Locate every uninfected red blood cell.
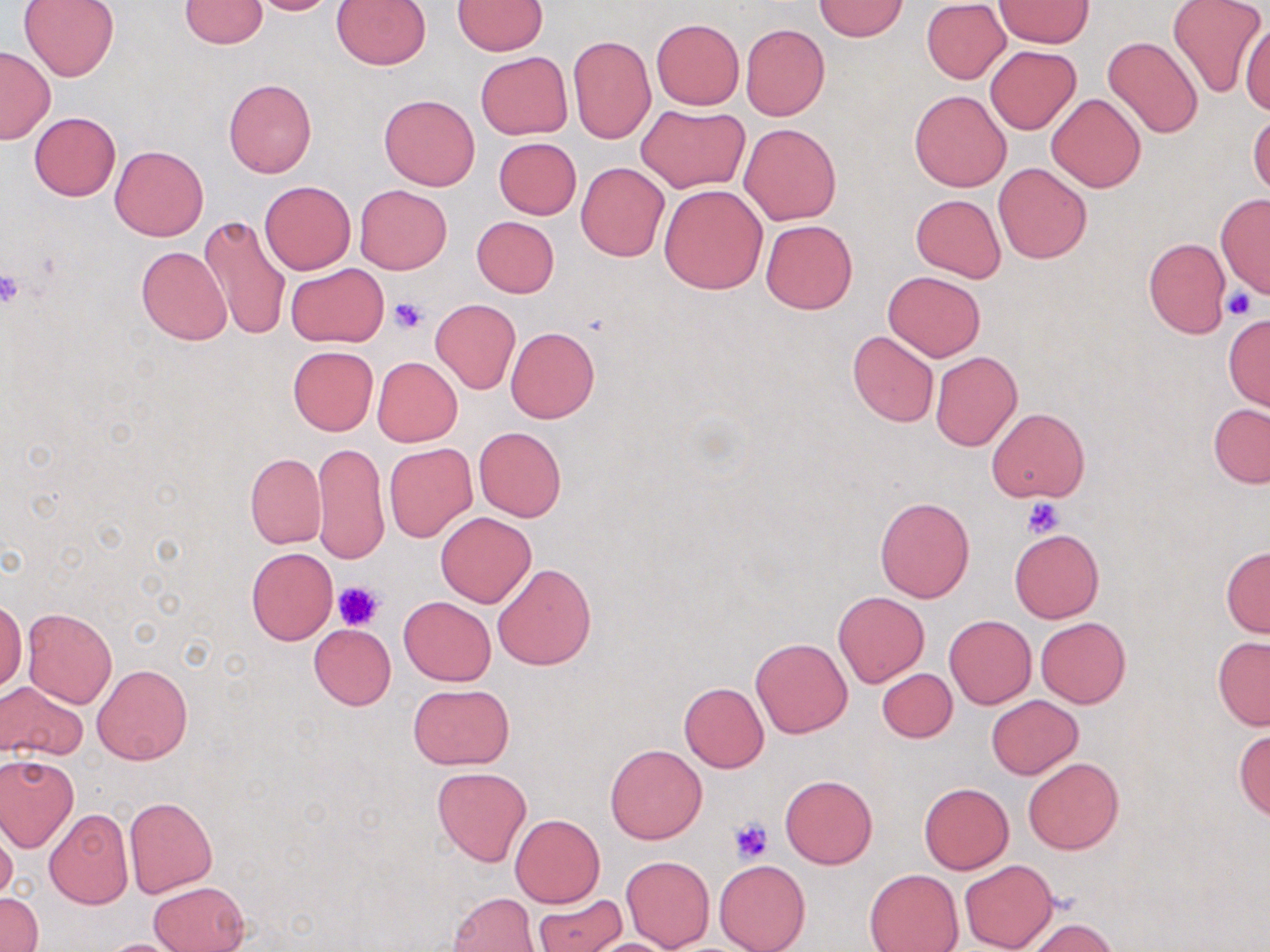

Approximate bounding boxes as named x1/y1/x2/y2 corners in pixels.
Uninfected red blood cells: (x1=18, y1=0, x2=120, y2=81), (x1=179, y1=0, x2=269, y2=48), (x1=245, y1=0, x2=340, y2=15), (x1=331, y1=1, x2=431, y2=70), (x1=453, y1=1, x2=548, y2=54), (x1=815, y1=1, x2=907, y2=41), (x1=995, y1=1, x2=1090, y2=48), (x1=1167, y1=1, x2=1266, y2=97), (x1=921, y1=2, x2=1010, y2=84), (x1=1241, y1=19, x2=1270, y2=116), (x1=651, y1=20, x2=744, y2=109), (x1=741, y1=23, x2=829, y2=120), (x1=568, y1=34, x2=655, y2=144), (x1=1103, y1=35, x2=1204, y2=139), (x1=986, y1=45, x2=1082, y2=135), (x1=0, y1=46, x2=56, y2=143), (x1=476, y1=52, x2=572, y2=138), (x1=224, y1=78, x2=316, y2=176), (x1=909, y1=90, x2=1011, y2=191), (x1=1046, y1=92, x2=1146, y2=193), (x1=379, y1=93, x2=480, y2=191), (x1=636, y1=105, x2=749, y2=193), (x1=1247, y1=111, x2=1270, y2=197), (x1=29, y1=113, x2=120, y2=200), (x1=739, y1=123, x2=841, y2=225), (x1=487, y1=137, x2=572, y2=296), (x1=494, y1=138, x2=581, y2=219), (x1=110, y1=144, x2=208, y2=240), (x1=992, y1=161, x2=1093, y2=264), (x1=576, y1=162, x2=668, y2=261), (x1=259, y1=181, x2=355, y2=274), (x1=660, y1=184, x2=767, y2=294), (x1=354, y1=185, x2=451, y2=274), (x1=1215, y1=193, x2=1270, y2=297), (x1=910, y1=194, x2=1006, y2=282), (x1=199, y1=214, x2=290, y2=339), (x1=472, y1=216, x2=559, y2=297), (x1=761, y1=219, x2=857, y2=314), (x1=1143, y1=237, x2=1230, y2=337), (x1=136, y1=246, x2=232, y2=344), (x1=286, y1=263, x2=388, y2=346), (x1=883, y1=271, x2=985, y2=361), (x1=429, y1=299, x2=521, y2=394), (x1=1223, y1=316, x2=1269, y2=411), (x1=505, y1=326, x2=599, y2=423), (x1=847, y1=331, x2=939, y2=428), (x1=288, y1=346, x2=378, y2=435), (x1=930, y1=351, x2=1022, y2=451), (x1=373, y1=357, x2=462, y2=446), (x1=1208, y1=404, x2=1270, y2=488), (x1=987, y1=407, x2=1089, y2=503), (x1=473, y1=427, x2=566, y2=521), (x1=313, y1=441, x2=387, y2=564), (x1=384, y1=443, x2=477, y2=542), (x1=245, y1=453, x2=326, y2=548), (x1=875, y1=496, x2=974, y2=603), (x1=435, y1=512, x2=536, y2=606), (x1=1010, y1=528, x2=1104, y2=623), (x1=1221, y1=547, x2=1270, y2=638), (x1=246, y1=548, x2=336, y2=644), (x1=492, y1=562, x2=597, y2=669), (x1=833, y1=591, x2=930, y2=687), (x1=399, y1=595, x2=496, y2=685), (x1=0, y1=600, x2=26, y2=691), (x1=21, y1=607, x2=117, y2=708), (x1=945, y1=615, x2=1035, y2=708), (x1=1036, y1=617, x2=1130, y2=708), (x1=309, y1=624, x2=396, y2=710), (x1=1212, y1=636, x2=1270, y2=730), (x1=751, y1=638, x2=852, y2=738), (x1=93, y1=663, x2=193, y2=765), (x1=877, y1=667, x2=958, y2=743), (x1=1, y1=682, x2=89, y2=760), (x1=679, y1=682, x2=769, y2=773), (x1=410, y1=683, x2=512, y2=769), (x1=987, y1=695, x2=1083, y2=779), (x1=1234, y1=726, x2=1270, y2=820), (x1=605, y1=743, x2=707, y2=844), (x1=0, y1=754, x2=80, y2=851), (x1=1023, y1=757, x2=1124, y2=854), (x1=432, y1=767, x2=531, y2=865), (x1=781, y1=774, x2=878, y2=868), (x1=920, y1=782, x2=1013, y2=874), (x1=123, y1=796, x2=217, y2=897), (x1=43, y1=809, x2=133, y2=909), (x1=510, y1=814, x2=605, y2=907), (x1=0, y1=825, x2=17, y2=902), (x1=621, y1=856, x2=715, y2=950), (x1=960, y1=858, x2=1058, y2=952), (x1=714, y1=860, x2=810, y2=952), (x1=865, y1=868, x2=964, y2=952), (x1=150, y1=881, x2=248, y2=951), (x1=0, y1=892, x2=42, y2=952), (x1=449, y1=892, x2=538, y2=952), (x1=533, y1=898, x2=626, y2=952), (x1=1025, y1=917, x2=1118, y2=952), (x1=580, y1=937, x2=684, y2=951), (x1=92, y1=939, x2=192, y2=952).

slide_level_diagnosis: no evidence of blood parasites
modality: optical microscopy
image_size: 1270×952 pixels
field_of_view: single
stain: May-Grünwald-Giemsa
magnification: 1000x
platelet_locations: 'approximate bounding boxes as named x1/y1/x2/y2 corners in pixels: (x1=0, y1=270, x2=24, y2=308), (x1=1222, y1=285, x2=1261, y2=320), (x1=389, y1=296, x2=430, y2=335), (x1=1022, y1=497, x2=1066, y2=538), (x1=333, y1=580, x2=383, y2=632), (x1=729, y1=818, x2=773, y2=864)'
preparation: thin blood film